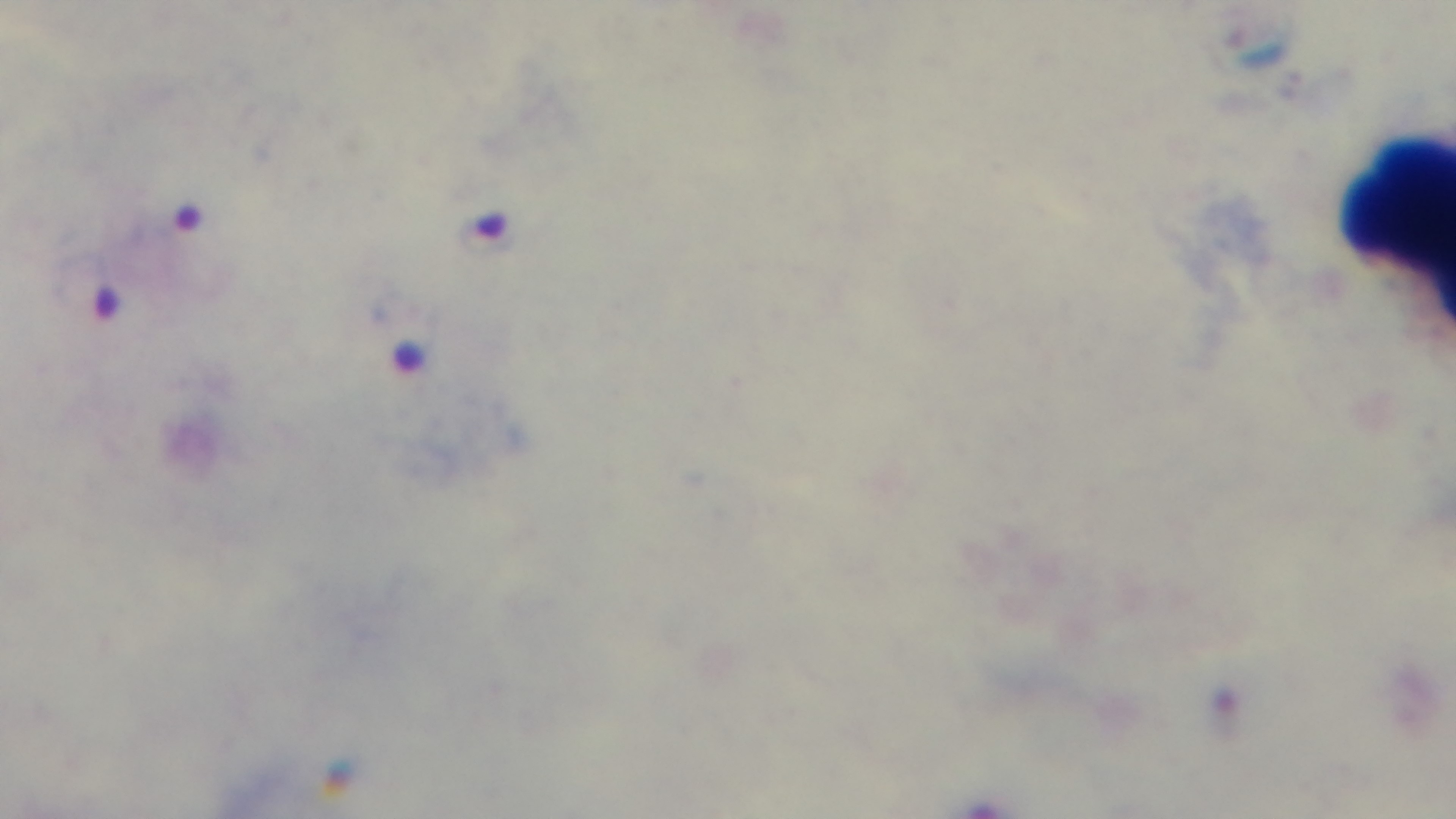

One field from the slide. Oil-immersion objective, 100x. Mounted 4K digital camera. Giemsa stain. Preparation: thick smear. Malaria status: infected. Light microscopy.